Locate Plasmodium parasites and leukocytes.
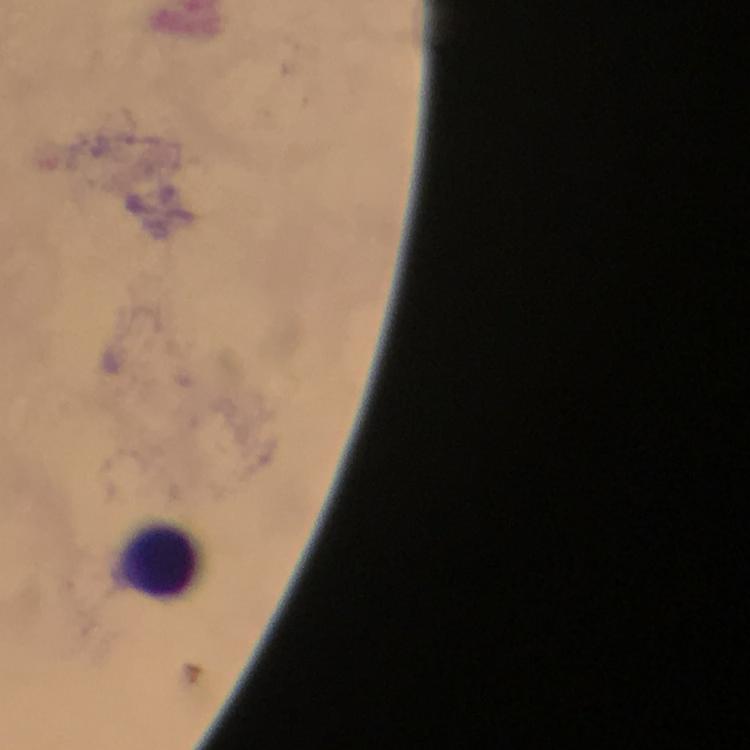
No Plasmodium parasites seen.
Approximate object centers, in pixels from the top-left corner.
Leukocytes: (x=162, y=562).

Summary:
  - Preparation: thick blood smear
  - Magnification: 100x
  - Capture: smartphone mounted on the microscope
  - Context: from a malaria diagnostic workup
  - Cropped from: one field of view
  - Immersion oil: used
  - Image size: 750×750 pixels
  - Stain: Giemsa